Describe the morphology of the erythrocytes.
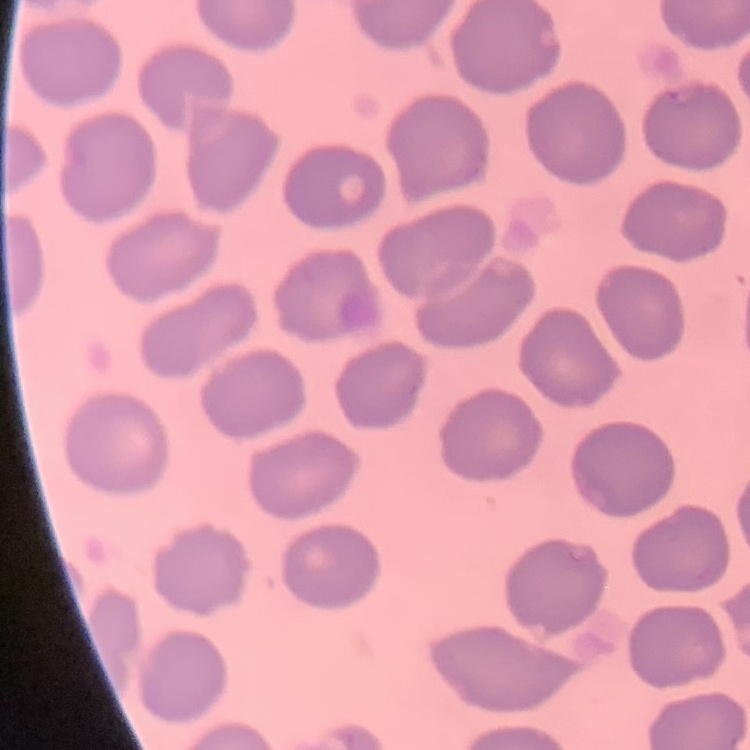

No rouleaux formation.

image type = one tile cut from a larger photomicrograph
stain = Field's or Giemsa
preparation = thin blood film